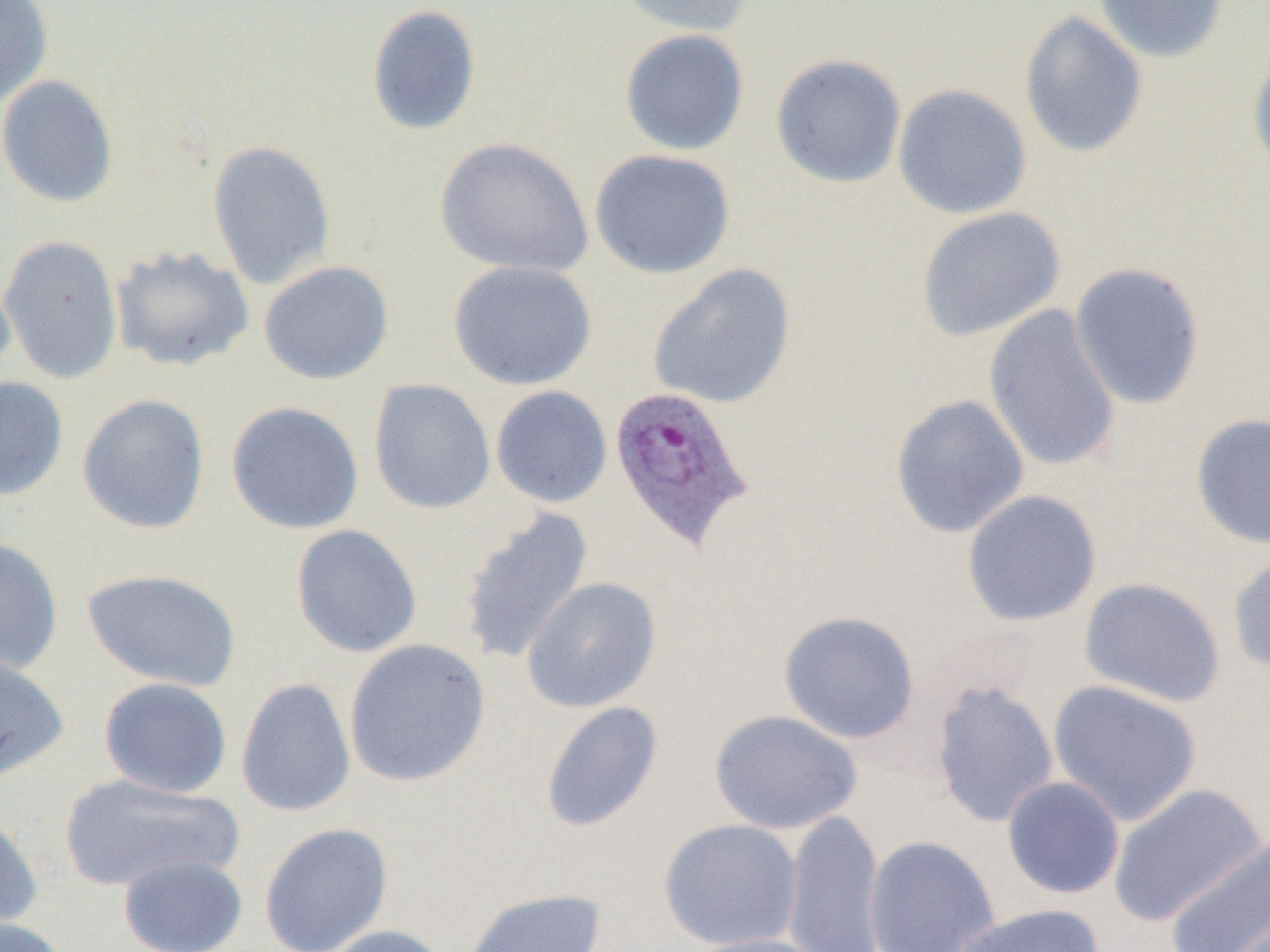

Approximate bounding boxes as named x1/y1/x2/y2 corners in pixels. Plasmodium ovale-infected red blood cell locations: (x1=607, y1=384, x2=756, y2=553). Uninfected red blood cell locations: (x1=0, y1=0, x2=53, y2=107), (x1=611, y1=0, x2=754, y2=38), (x1=1093, y1=0, x2=1230, y2=63), (x1=366, y1=4, x2=482, y2=136), (x1=1018, y1=10, x2=1148, y2=158), (x1=619, y1=28, x2=750, y2=156), (x1=1247, y1=41, x2=1270, y2=181), (x1=770, y1=53, x2=907, y2=189), (x1=0, y1=75, x2=118, y2=208), (x1=892, y1=83, x2=1033, y2=220), (x1=434, y1=137, x2=595, y2=278), (x1=206, y1=139, x2=336, y2=289), (x1=589, y1=149, x2=736, y2=279), (x1=915, y1=206, x2=1065, y2=342), (x1=0, y1=234, x2=123, y2=384), (x1=110, y1=245, x2=255, y2=372), (x1=258, y1=259, x2=394, y2=385), (x1=448, y1=260, x2=598, y2=391), (x1=1069, y1=261, x2=1206, y2=410), (x1=648, y1=263, x2=797, y2=409), (x1=0, y1=267, x2=16, y2=385), (x1=984, y1=304, x2=1122, y2=473), (x1=0, y1=375, x2=69, y2=501), (x1=368, y1=378, x2=496, y2=515), (x1=491, y1=385, x2=613, y2=508), (x1=77, y1=393, x2=211, y2=534), (x1=889, y1=393, x2=1030, y2=538), (x1=226, y1=400, x2=365, y2=534), (x1=1189, y1=412, x2=1270, y2=551), (x1=961, y1=489, x2=1103, y2=627), (x1=457, y1=506, x2=595, y2=665), (x1=290, y1=524, x2=422, y2=658), (x1=0, y1=538, x2=64, y2=677), (x1=1227, y1=551, x2=1270, y2=675), (x1=81, y1=568, x2=242, y2=692), (x1=521, y1=577, x2=662, y2=713), (x1=1078, y1=577, x2=1226, y2=708), (x1=777, y1=609, x2=920, y2=743), (x1=344, y1=639, x2=492, y2=787), (x1=0, y1=653, x2=69, y2=784), (x1=98, y1=677, x2=233, y2=798), (x1=235, y1=677, x2=356, y2=818), (x1=1047, y1=679, x2=1203, y2=827), (x1=929, y1=681, x2=1059, y2=828), (x1=540, y1=700, x2=664, y2=833), (x1=709, y1=709, x2=863, y2=834), (x1=59, y1=773, x2=242, y2=892), (x1=1002, y1=776, x2=1126, y2=899), (x1=1107, y1=782, x2=1267, y2=928), (x1=782, y1=809, x2=887, y2=952), (x1=0, y1=811, x2=44, y2=934), (x1=659, y1=818, x2=803, y2=950), (x1=259, y1=822, x2=394, y2=952), (x1=863, y1=834, x2=1001, y2=952), (x1=1164, y1=835, x2=1270, y2=952), (x1=118, y1=852, x2=248, y2=952), (x1=460, y1=888, x2=608, y2=952), (x1=949, y1=903, x2=1107, y2=952), (x1=1216, y1=908, x2=1269, y2=952), (x1=0, y1=917, x2=70, y2=952), (x1=322, y1=924, x2=451, y2=952), (x1=685, y1=933, x2=830, y2=952). Slide-level diagnosis: Plasmodium ovale. Thin blood smear. Captured at 1000x magnification. One field of a larger specimen. Light microscopy. Image is 1270×952 pixels.